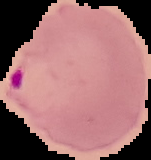
image size = 151×160 pixels
malaria status = parasitized
image type = cell region segmented out of the field of view; surrounding area masked to black
preparation = thin blood smear